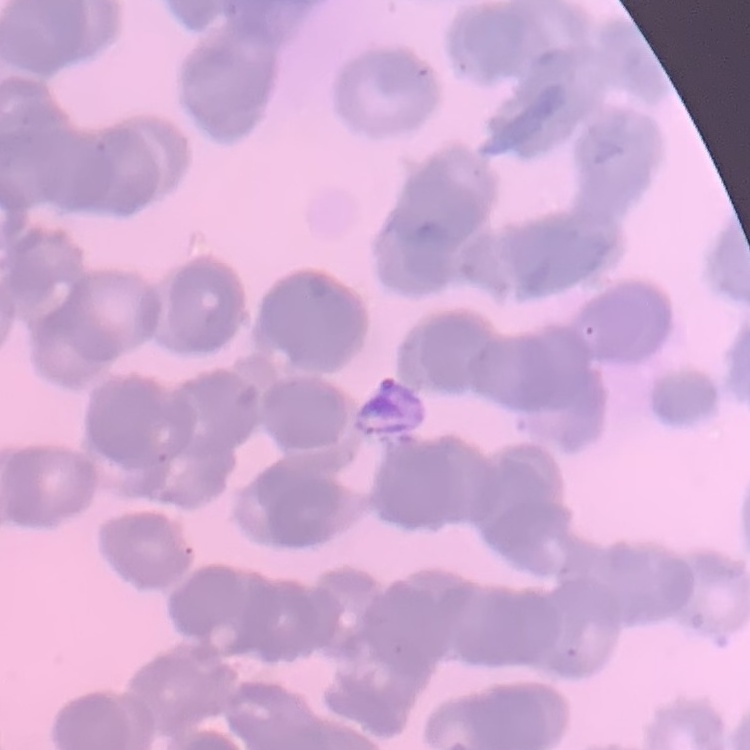
Summary:
  - Erythrocyte morphology: rouleaux formation
  - Image type: square crop of a larger photomicrograph
  - Preparation: thin peripheral smear
  - Stain: Field's or Giemsa